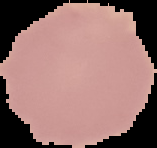

Summary:
  - Image size: 157×148 pixels
  - Result: negative for malaria parasites
  - Preparation: thin blood film
  - Image type: segmented cell region on a black background